Locate every Plasmodium falciparum-infected red blood cell.
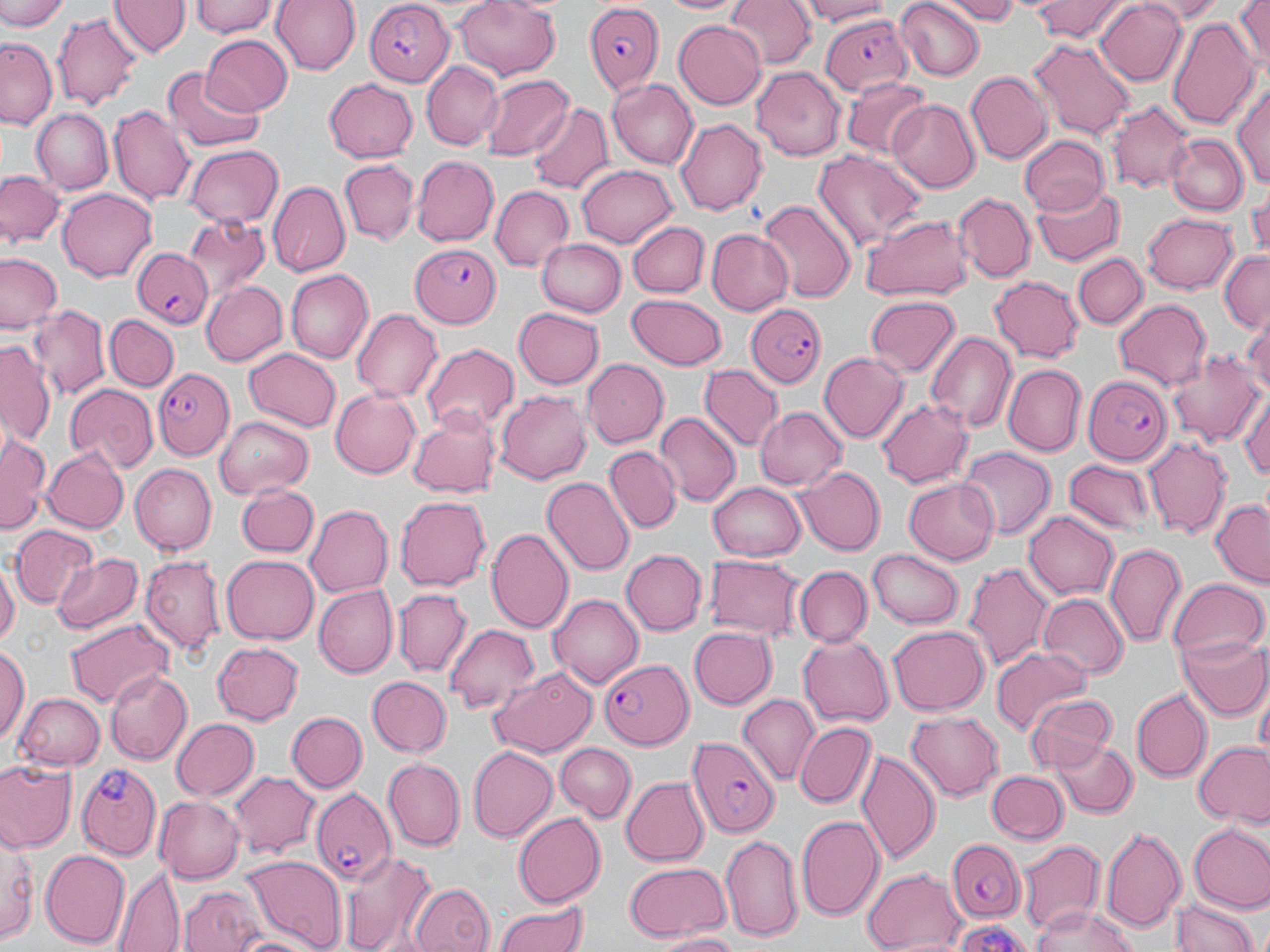
Approximate bounding boxes as named x1/y1/x2/y2 corners in pixels.
Plasmodium falciparum-infected red blood cells: (x1=583, y1=0, x2=664, y2=91), (x1=361, y1=3, x2=451, y2=84), (x1=819, y1=15, x2=911, y2=97), (x1=411, y1=240, x2=503, y2=329), (x1=132, y1=247, x2=212, y2=332), (x1=748, y1=300, x2=827, y2=389), (x1=153, y1=367, x2=234, y2=459), (x1=1083, y1=375, x2=1170, y2=465), (x1=593, y1=651, x2=696, y2=753), (x1=689, y1=736, x2=779, y2=838), (x1=75, y1=762, x2=162, y2=856), (x1=309, y1=784, x2=396, y2=887), (x1=947, y1=837, x2=1025, y2=924).

Uninfected red blood cell locations: (x1=1, y1=0, x2=67, y2=32), (x1=110, y1=0, x2=188, y2=59), (x1=189, y1=0, x2=280, y2=38), (x1=268, y1=0, x2=359, y2=75), (x1=658, y1=0, x2=748, y2=17), (x1=727, y1=0, x2=815, y2=69), (x1=797, y1=0, x2=896, y2=24), (x1=896, y1=0, x2=985, y2=80), (x1=939, y1=0, x2=1021, y2=22), (x1=1026, y1=0, x2=1131, y2=42), (x1=1142, y1=0, x2=1227, y2=21), (x1=1231, y1=0, x2=1270, y2=77), (x1=452, y1=1, x2=561, y2=79), (x1=1093, y1=2, x2=1187, y2=88), (x1=1167, y1=12, x2=1259, y2=132), (x1=55, y1=14, x2=141, y2=108), (x1=673, y1=20, x2=766, y2=108), (x1=200, y1=35, x2=292, y2=117), (x1=0, y1=38, x2=59, y2=129), (x1=1031, y1=40, x2=1135, y2=140), (x1=423, y1=61, x2=503, y2=148), (x1=751, y1=67, x2=846, y2=160), (x1=161, y1=69, x2=266, y2=153), (x1=965, y1=71, x2=1050, y2=165), (x1=479, y1=72, x2=575, y2=160), (x1=1233, y1=76, x2=1270, y2=195), (x1=324, y1=77, x2=418, y2=163), (x1=840, y1=77, x2=930, y2=158), (x1=607, y1=78, x2=699, y2=168), (x1=886, y1=100, x2=979, y2=193), (x1=1106, y1=101, x2=1194, y2=194), (x1=527, y1=102, x2=614, y2=195), (x1=108, y1=105, x2=194, y2=206), (x1=29, y1=108, x2=114, y2=194), (x1=675, y1=118, x2=766, y2=215), (x1=1016, y1=134, x2=1112, y2=214), (x1=1168, y1=135, x2=1247, y2=215), (x1=183, y1=144, x2=284, y2=230), (x1=811, y1=149, x2=924, y2=251), (x1=409, y1=155, x2=497, y2=247), (x1=339, y1=160, x2=419, y2=246), (x1=577, y1=162, x2=677, y2=246), (x1=0, y1=170, x2=66, y2=250), (x1=267, y1=180, x2=351, y2=278), (x1=1031, y1=182, x2=1124, y2=267), (x1=489, y1=185, x2=574, y2=273), (x1=1248, y1=187, x2=1270, y2=258), (x1=57, y1=189, x2=155, y2=282), (x1=952, y1=192, x2=1035, y2=282), (x1=759, y1=200, x2=856, y2=304), (x1=861, y1=212, x2=975, y2=301), (x1=1141, y1=213, x2=1240, y2=294), (x1=185, y1=218, x2=269, y2=304), (x1=630, y1=222, x2=709, y2=297), (x1=706, y1=230, x2=794, y2=314), (x1=534, y1=238, x2=625, y2=317), (x1=1217, y1=250, x2=1270, y2=333), (x1=2, y1=252, x2=63, y2=335), (x1=1074, y1=252, x2=1146, y2=330), (x1=283, y1=270, x2=371, y2=363), (x1=989, y1=274, x2=1084, y2=362), (x1=201, y1=280, x2=289, y2=365), (x1=624, y1=294, x2=728, y2=369), (x1=864, y1=295, x2=961, y2=379), (x1=1112, y1=298, x2=1212, y2=393), (x1=29, y1=305, x2=110, y2=402), (x1=512, y1=307, x2=605, y2=390), (x1=352, y1=308, x2=441, y2=403), (x1=106, y1=315, x2=177, y2=390), (x1=1241, y1=315, x2=1270, y2=406), (x1=926, y1=328, x2=1016, y2=433), (x1=1, y1=338, x2=55, y2=449), (x1=422, y1=344, x2=518, y2=435), (x1=243, y1=348, x2=341, y2=433), (x1=1167, y1=348, x2=1265, y2=445), (x1=820, y1=352, x2=907, y2=442), (x1=582, y1=360, x2=669, y2=448), (x1=1001, y1=365, x2=1083, y2=456), (x1=699, y1=366, x2=781, y2=452), (x1=1237, y1=380, x2=1270, y2=489), (x1=65, y1=384, x2=157, y2=474), (x1=330, y1=389, x2=421, y2=478), (x1=494, y1=391, x2=591, y2=484), (x1=876, y1=398, x2=972, y2=489), (x1=756, y1=405, x2=847, y2=491), (x1=406, y1=411, x2=501, y2=500), (x1=655, y1=411, x2=740, y2=505), (x1=214, y1=416, x2=312, y2=498), (x1=0, y1=434, x2=50, y2=529), (x1=1141, y1=437, x2=1230, y2=540), (x1=604, y1=446, x2=680, y2=532), (x1=42, y1=447, x2=130, y2=535), (x1=958, y1=447, x2=1056, y2=541), (x1=1063, y1=459, x2=1158, y2=536), (x1=130, y1=463, x2=216, y2=554), (x1=795, y1=466, x2=883, y2=554), (x1=540, y1=477, x2=634, y2=576), (x1=904, y1=480, x2=999, y2=564), (x1=707, y1=481, x2=805, y2=561), (x1=233, y1=482, x2=320, y2=558), (x1=393, y1=494, x2=491, y2=591), (x1=1210, y1=499, x2=1269, y2=589), (x1=305, y1=502, x2=394, y2=597), (x1=1024, y1=509, x2=1118, y2=597), (x1=10, y1=526, x2=99, y2=611), (x1=487, y1=528, x2=574, y2=635), (x1=1104, y1=542, x2=1186, y2=648), (x1=867, y1=547, x2=964, y2=627), (x1=620, y1=549, x2=707, y2=636), (x1=50, y1=552, x2=144, y2=638), (x1=707, y1=553, x2=804, y2=640), (x1=139, y1=555, x2=224, y2=658), (x1=221, y1=555, x2=320, y2=645), (x1=0, y1=560, x2=18, y2=654), (x1=965, y1=560, x2=1055, y2=673), (x1=793, y1=565, x2=871, y2=645), (x1=1166, y1=580, x2=1266, y2=671), (x1=312, y1=584, x2=398, y2=677), (x1=393, y1=589, x2=471, y2=676), (x1=549, y1=592, x2=643, y2=688), (x1=1039, y1=593, x2=1129, y2=678), (x1=65, y1=617, x2=171, y2=711), (x1=445, y1=623, x2=542, y2=713), (x1=888, y1=626, x2=988, y2=716), (x1=690, y1=627, x2=775, y2=709), (x1=1177, y1=631, x2=1270, y2=719), (x1=798, y1=635, x2=893, y2=726), (x1=210, y1=641, x2=306, y2=724), (x1=1, y1=642, x2=29, y2=742), (x1=992, y1=647, x2=1090, y2=735), (x1=488, y1=666, x2=598, y2=756), (x1=105, y1=669, x2=192, y2=766), (x1=366, y1=676, x2=451, y2=757), (x1=1256, y1=687, x2=1269, y2=764), (x1=1131, y1=688, x2=1210, y2=781), (x1=13, y1=692, x2=104, y2=771), (x1=1026, y1=692, x2=1120, y2=772), (x1=737, y1=695, x2=821, y2=785), (x1=287, y1=710, x2=366, y2=792), (x1=905, y1=712, x2=1004, y2=803), (x1=169, y1=717, x2=258, y2=801), (x1=795, y1=722, x2=875, y2=808), (x1=1052, y1=738, x2=1136, y2=818), (x1=1192, y1=741, x2=1269, y2=826), (x1=554, y1=743, x2=635, y2=823), (x1=468, y1=745, x2=558, y2=841), (x1=856, y1=748, x2=940, y2=868), (x1=382, y1=757, x2=465, y2=852), (x1=0, y1=760, x2=74, y2=851), (x1=229, y1=770, x2=321, y2=859), (x1=984, y1=771, x2=1068, y2=844), (x1=620, y1=777, x2=708, y2=866), (x1=153, y1=795, x2=244, y2=883), (x1=513, y1=812, x2=606, y2=906), (x1=796, y1=814, x2=885, y2=921), (x1=1, y1=825, x2=38, y2=948), (x1=1188, y1=825, x2=1270, y2=915), (x1=1103, y1=827, x2=1188, y2=933), (x1=720, y1=832, x2=802, y2=942), (x1=1018, y1=838, x2=1103, y2=939), (x1=40, y1=848, x2=131, y2=949), (x1=339, y1=851, x2=437, y2=952), (x1=245, y1=856, x2=344, y2=947), (x1=621, y1=861, x2=731, y2=942), (x1=864, y1=866, x2=968, y2=950), (x1=117, y1=870, x2=186, y2=952), (x1=181, y1=882, x2=268, y2=952), (x1=407, y1=883, x2=494, y2=952), (x1=1172, y1=897, x2=1260, y2=952), (x1=493, y1=900, x2=592, y2=952), (x1=1032, y1=906, x2=1141, y2=952), (x1=947, y1=920, x2=1032, y2=952), (x1=227, y1=931, x2=321, y2=952), (x1=652, y1=931, x2=746, y2=951). Slide-level diagnosis: Plasmodium falciparum. May-Grünwald-Giemsa stain. Optical microscopy. Captured at 1000x magnification. One field of a larger specimen. Image is 1270×952 pixels. Thin blood film.